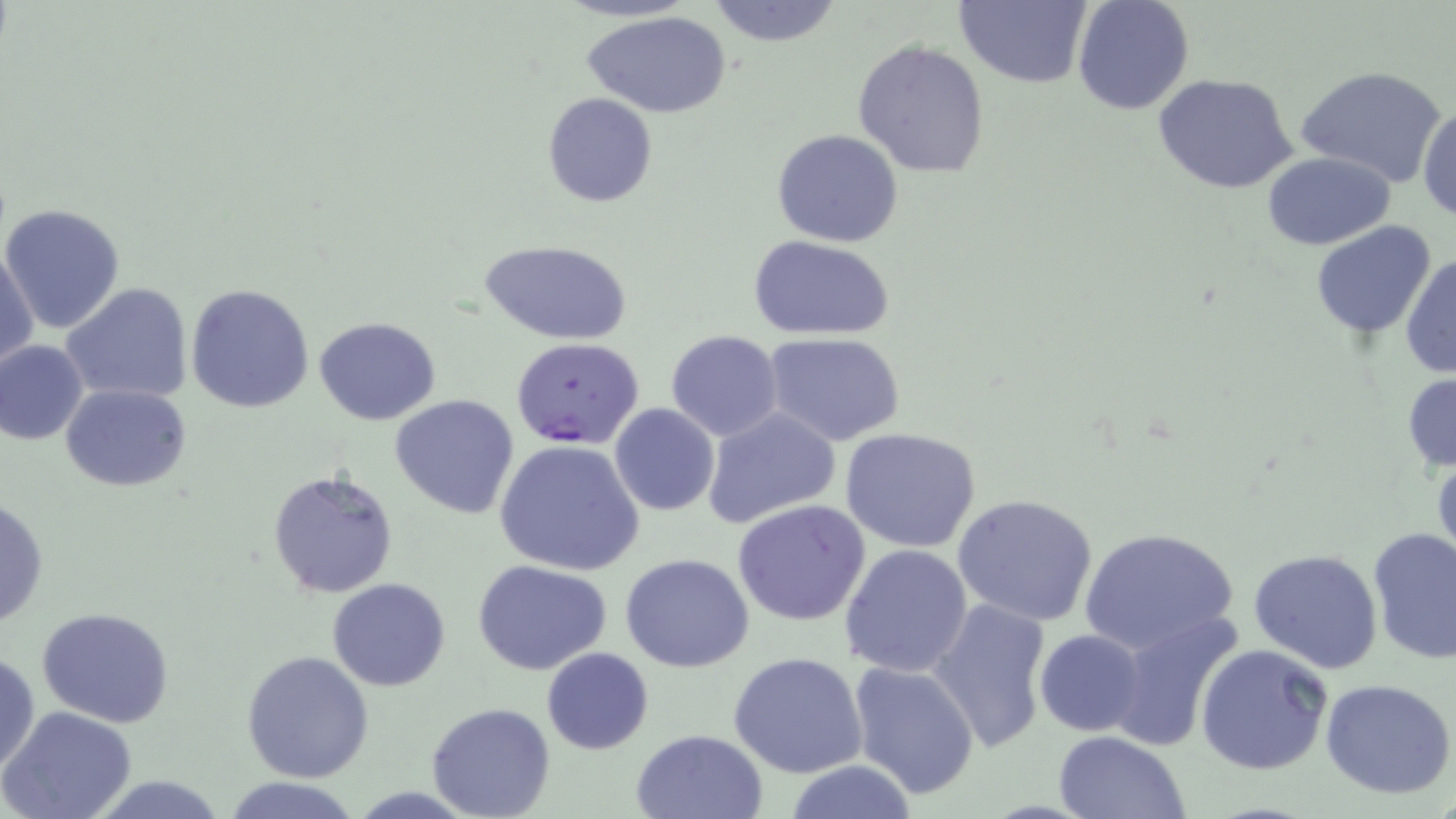
Summary:
  - Coordinate format: approximate bounding boxes as (x1, y1, x2, y2) in pixels
  - Uninfected red blood cell locations: (705, 0, 845, 49), (955, 0, 1094, 89), (1073, 0, 1195, 116), (581, 9, 733, 117), (853, 38, 991, 179), (1295, 66, 1447, 189), (1153, 72, 1299, 194), (541, 94, 658, 207), (1418, 102, 1455, 226), (771, 127, 903, 248), (1263, 152, 1395, 249), (1, 203, 126, 334), (1310, 221, 1437, 337), (750, 237, 894, 341), (483, 240, 629, 346), (1, 247, 39, 372), (1400, 251, 1455, 379), (60, 281, 193, 404), (185, 283, 315, 414), (314, 316, 440, 424), (664, 330, 783, 442), (763, 332, 908, 446), (0, 339, 89, 445), (715, 353, 879, 512), (1402, 370, 1456, 476), (61, 384, 191, 491), (391, 394, 521, 518), (609, 404, 721, 516), (702, 406, 841, 531), (839, 426, 986, 554), (496, 440, 646, 578), (1430, 443, 1455, 571), (267, 468, 399, 598), (953, 494, 1100, 627), (0, 495, 49, 631), (733, 499, 872, 628), (1078, 527, 1239, 659), (1367, 527, 1456, 665), (839, 543, 973, 677), (1248, 549, 1384, 675), (620, 553, 755, 672), (472, 559, 614, 676), (327, 578, 451, 691), (927, 598, 1054, 752), (35, 606, 177, 728), (1107, 611, 1244, 753), (1034, 629, 1147, 737), (1195, 643, 1333, 776), (541, 647, 653, 754), (1, 649, 39, 780), (242, 649, 374, 781), (728, 652, 869, 779), (849, 660, 981, 801), (1321, 678, 1456, 800), (428, 703, 555, 818), (2, 707, 137, 819), (630, 728, 769, 819), (1051, 732, 1191, 819), (783, 760, 920, 818), (217, 777, 368, 818)
  - Plasmodium falciparum-infected red blood cell locations: (510, 337, 644, 451)
  - Slide-level diagnosis: Plasmodium falciparum
  - Field of view: one of a larger specimen
  - Modality: light microscopy
  - Image size: 1456×819 pixels
  - Stain: May-Grünwald-Giemsa
  - Magnification: 1000x
  - Preparation: thin blood smear